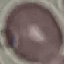

Summary:
  - Result: negative for malaria parasites
  - Stain: Giemsa
  - Image type: automatically extracted cell patch, resized to 64 × 64 pixels
  - Capture: smartphone camera at the microscope eyepiece
  - Preparation: thin smear